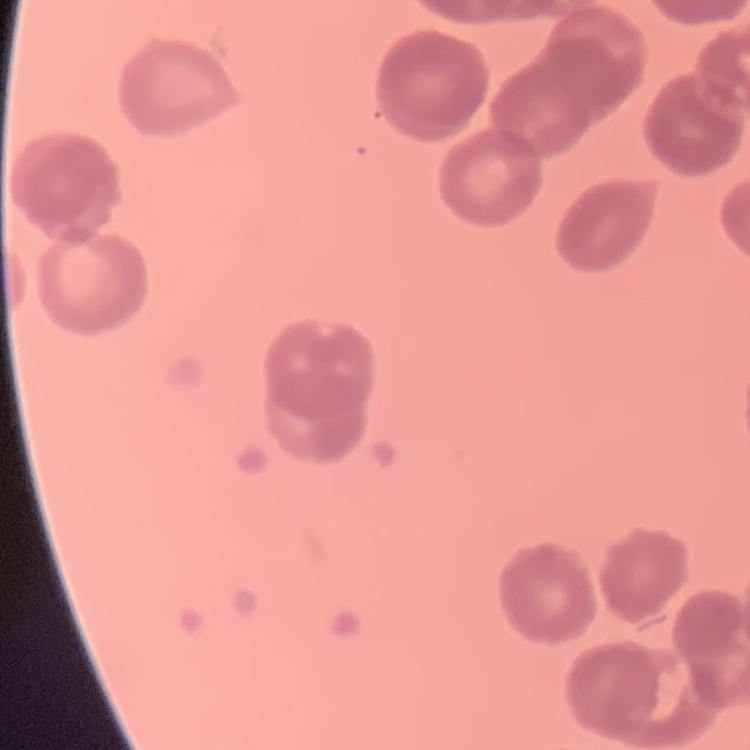
red blood cell morphology = rouleaux formation
preparation = thin peripheral smear
stain = Field's or Giemsa
image type = one tile cut from a larger photomicrograph